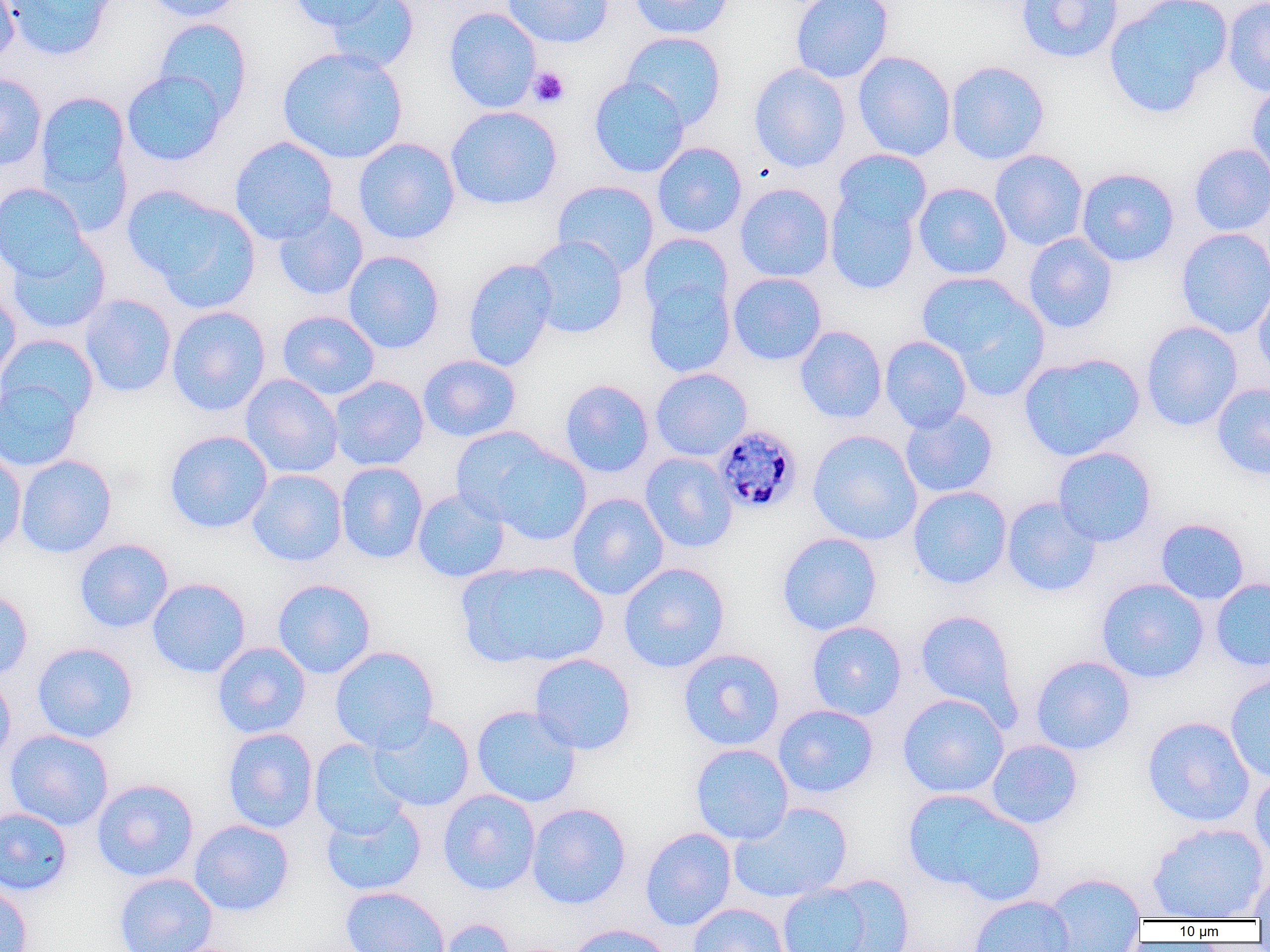

Summary:
  - Coordinate format: approximate bounding boxes as [x1, y1, x2, y2] in pixels
  - Uninfected red blood cell locations: [0, 0, 20, 65], [4, 0, 116, 61], [143, 0, 247, 22], [289, 0, 390, 32], [324, 0, 419, 73], [502, 0, 613, 48], [629, 0, 734, 39], [790, 0, 894, 84], [1016, 0, 1124, 64], [1103, 0, 1232, 118], [1222, 0, 1270, 97], [444, 7, 541, 113], [153, 18, 253, 120], [621, 31, 727, 129], [276, 46, 409, 164], [853, 51, 956, 161], [945, 60, 1050, 164], [749, 63, 851, 172], [121, 70, 228, 166], [0, 72, 47, 171], [589, 76, 689, 178], [1246, 82, 1270, 186], [34, 92, 132, 212], [445, 105, 563, 210], [229, 136, 339, 244], [353, 138, 460, 244], [652, 142, 747, 238], [1188, 143, 1270, 236], [833, 149, 932, 234], [990, 149, 1088, 251], [1076, 167, 1179, 267], [552, 180, 659, 277], [0, 182, 90, 281], [913, 182, 1012, 280], [734, 183, 835, 282], [126, 187, 260, 310], [825, 187, 922, 295], [273, 207, 368, 301], [1175, 227, 1270, 339], [638, 233, 733, 322], [1023, 233, 1118, 333], [5, 236, 111, 335], [526, 236, 629, 339], [342, 250, 445, 354], [463, 257, 559, 372], [727, 272, 827, 365], [918, 272, 1047, 393], [642, 275, 735, 378], [1253, 280, 1270, 385], [0, 288, 21, 385], [78, 293, 177, 398], [166, 306, 271, 416], [277, 310, 380, 400], [1141, 321, 1243, 431], [795, 326, 887, 424], [0, 334, 99, 424], [879, 335, 971, 433], [1019, 352, 1146, 461], [418, 354, 521, 442], [650, 368, 752, 461], [240, 374, 343, 478], [328, 375, 429, 471], [0, 378, 83, 472], [560, 379, 654, 478], [1211, 382, 1270, 480], [900, 407, 999, 498], [164, 430, 273, 534], [807, 430, 923, 545], [473, 439, 592, 546], [1052, 446, 1157, 547], [0, 448, 26, 555], [640, 452, 738, 554], [15, 454, 117, 558], [336, 462, 429, 564], [246, 469, 348, 567], [907, 486, 1012, 589], [411, 487, 510, 582], [567, 492, 669, 600], [1001, 496, 1101, 597], [1156, 518, 1249, 604], [776, 532, 882, 636], [74, 538, 174, 633], [458, 560, 609, 670], [618, 562, 730, 673], [147, 577, 251, 678], [1096, 577, 1209, 683], [272, 578, 376, 679], [1211, 578, 1270, 672], [0, 588, 33, 680], [914, 609, 1020, 720], [806, 621, 907, 721], [32, 642, 139, 743], [212, 642, 311, 739], [330, 645, 439, 752], [677, 648, 786, 751], [529, 653, 637, 755], [1030, 655, 1136, 755], [0, 670, 16, 768], [1225, 672, 1270, 784], [897, 692, 1009, 798], [471, 704, 582, 807], [773, 704, 879, 798], [367, 713, 475, 812], [1142, 715, 1256, 827], [222, 728, 319, 833], [5, 729, 114, 831], [309, 739, 410, 839], [986, 739, 1083, 829], [690, 743, 794, 845], [1249, 771, 1270, 867], [91, 778, 199, 882], [438, 788, 541, 895], [902, 788, 1046, 904], [320, 801, 426, 897], [526, 802, 631, 909], [728, 802, 853, 904], [0, 807, 72, 896], [189, 819, 294, 916], [1146, 822, 1269, 920], [640, 827, 736, 931], [1248, 869, 1270, 920], [113, 872, 217, 952], [1041, 872, 1149, 951], [816, 873, 916, 952], [775, 880, 883, 952], [0, 881, 33, 952], [340, 886, 451, 952], [969, 894, 1075, 952], [687, 902, 790, 952], [435, 918, 517, 952], [565, 923, 674, 952]
  - Platelet locations: [528, 67, 570, 108]
  - Plasmodium malariae-infected red blood cell locations: [713, 424, 804, 515]
  - Slide-level diagnosis: Plasmodium malariae
  - Image size: 1270×952 pixels
  - Magnification: 1000x
  - Preparation: thin blood film
  - Field of view: one of a larger specimen
  - Modality: optical microscopy